State which parasite is depicted.
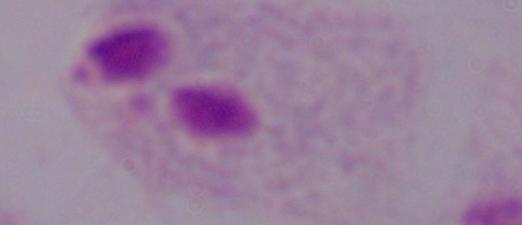

This is a trichomonad.

Summary:
  - Magnification: 1000x
  - Modality: micrograph